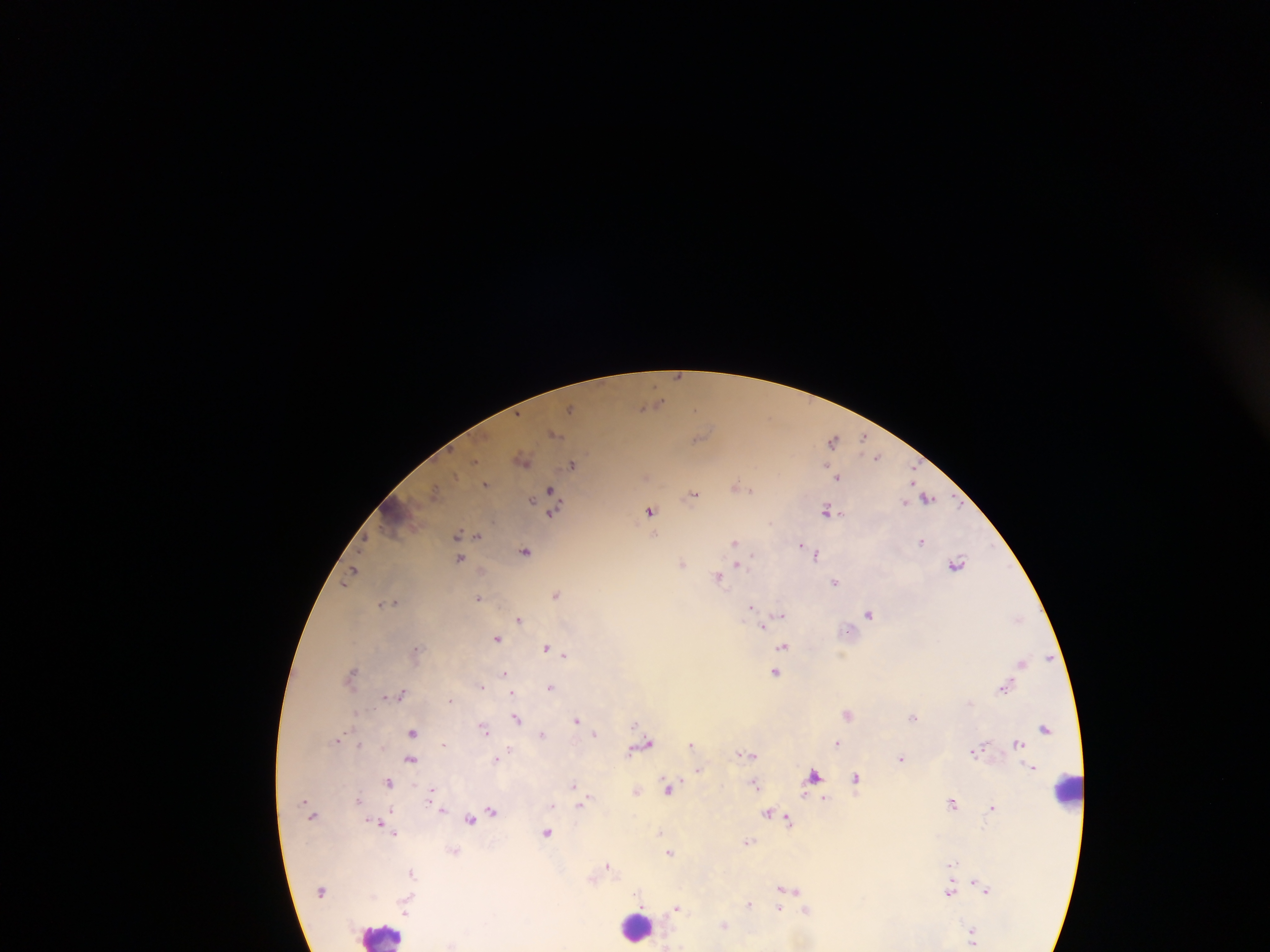

{
  "capture": "mobile-phone photograph through a microscope",
  "country": "Ghana",
  "image_size": "1270×952 pixels",
  "preparation": "thick blood film",
  "field_of_view": "single",
  "malaria_parasite_locations": "approximate centers as x y in pixels: 676 376; 572 407; 698 407; 862 437; 832 438; 877 455; 477 464; 573 465; 914 473; 837 478; 485 484; 549 488; 752 489; 693 495; 926 498; 827 509; 649 510; 552 512; 457 534; 477 535; 922 541; 735 542; 799 544; 525 550; 816 554; 460 558; 957 562; 737 565; 353 569; 718 577; 836 581; 556 594; 479 597; 380 604; 750 608; 868 614; 780 615; 520 617; 764 623; 497 638; 783 646; 545 647; 564 654; 1021 662; 352 670; 504 671; 775 671; 481 684; 551 686; 1004 688; 511 689; 401 693; 511 694; 384 695; 450 700; 972 704; 352 712; 848 714; 914 717; 576 719; 515 720; 634 723; 485 730; 595 731; 412 732; 543 734; 336 740; 691 741; 443 742; 837 743; 358 744; 641 745; 510 749; 972 751; 745 753; 901 756; 495 758; 410 759; 698 770; 856 779; 755 782; 388 783; 575 783; 669 786; 431 789; 638 789; 358 800; 587 800; 953 802; 579 804; 993 807; 387 809; 441 809; 492 811; 769 814; 471 819; 788 820; 377 822; 661 831; 547 832; 394 834; 749 842; 672 851; 953 863; 609 866; 410 871; 786 890; 948 892; 748 903; 780 906; 677 908; 725 926",
  "leukocyte_locations": "approximate centers as x y in pixels: 1064 791; 639 928; 379 934"
}